Report the malaria status.
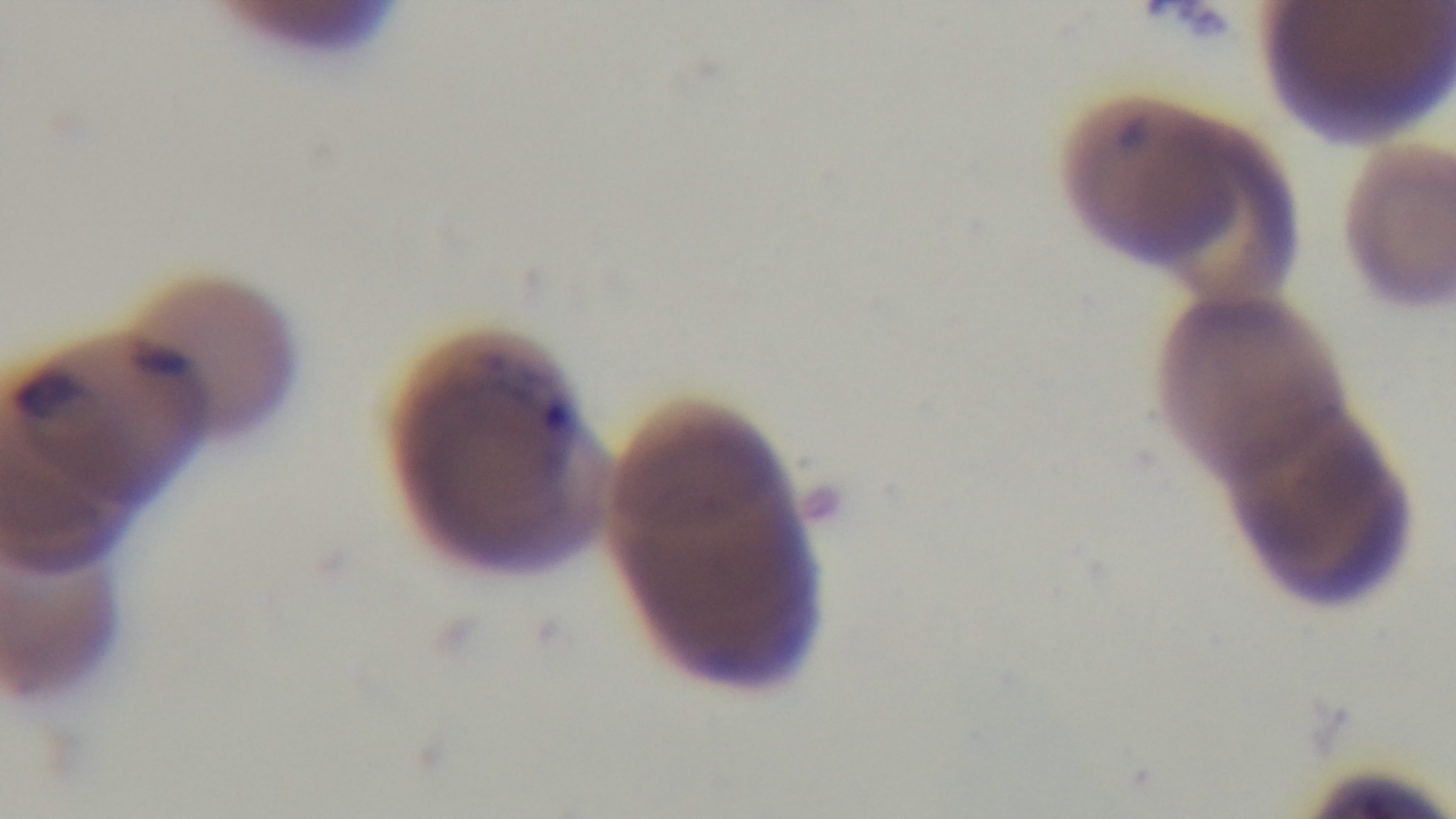

Infected.

Single field of view. Giemsa-stained. Light microscopy. Preparation: thin smear. 100x oil-immersion objective. Captured with a mounted 4K digital camera.